Name the parasite shown.
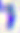

Toxoplasma gondii.

Summary:
  - Magnification: 400x
  - Modality: micrograph